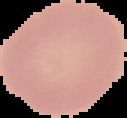
Summary:
  - Malaria status: uninfected
  - Preparation: thin blood smear
  - Image type: segmented cell region with the area outside set to black
  - Image size: 127×118 pixels